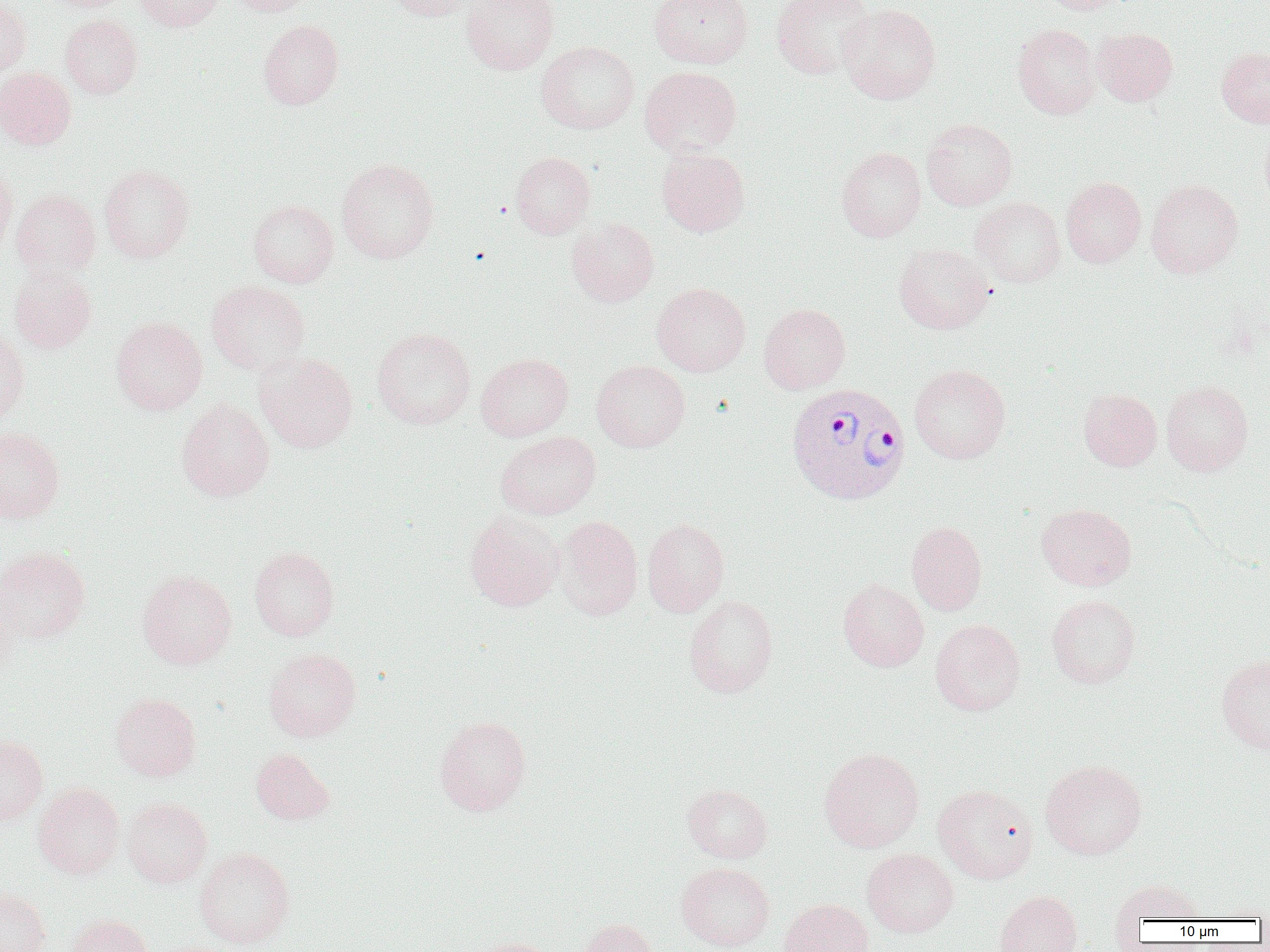

{
  "plasmodium_vivax_infected_red_blood_cell_locations": "approximate bounding boxes as (x1, y1, x2, y2) in pixels: (786, 382, 910, 505)",
  "slide_level_diagnosis": "Plasmodium vivax",
  "modality": "optical microscopy",
  "image_size": "1270×952 pixels",
  "preparation": "thin blood smear",
  "magnification": "1000x",
  "field_of_view": "single",
  "uninfected_red_blood_cell_locations": "approximate bounding boxes as (x1, y1, x2, y2) in pixels: (40, 0, 132, 12), (133, 0, 225, 31), (227, 0, 315, 16), (389, 0, 476, 21), (462, 0, 559, 75), (649, 0, 753, 69), (771, 0, 874, 79), (1039, 0, 1131, 15), (0, 1, 30, 80), (838, 3, 941, 104), (60, 14, 142, 99), (258, 19, 344, 109), (1013, 24, 1102, 118), (1092, 27, 1178, 106), (536, 41, 640, 134), (1216, 46, 1270, 127), (640, 66, 742, 157), (0, 67, 76, 150), (921, 118, 1017, 211), (1259, 119, 1270, 212), (837, 146, 926, 242), (656, 148, 750, 236), (510, 151, 595, 238), (337, 158, 439, 263), (99, 163, 195, 264), (0, 164, 17, 261), (1061, 177, 1146, 268), (1146, 179, 1243, 278), (11, 189, 101, 281), (970, 196, 1066, 288), (248, 199, 339, 287), (566, 218, 659, 307), (893, 243, 995, 334), (9, 267, 97, 354), (207, 280, 311, 375), (652, 282, 751, 376), (759, 303, 851, 393), (111, 317, 208, 414), (0, 325, 29, 423), (372, 328, 475, 429), (254, 352, 358, 453), (475, 353, 573, 441), (592, 360, 690, 452), (909, 363, 1011, 463), (1161, 381, 1253, 476), (1078, 388, 1162, 470), (176, 398, 274, 501), (0, 427, 65, 523), (495, 432, 601, 520), (1036, 503, 1136, 590), (464, 510, 564, 612), (554, 515, 643, 620), (642, 518, 730, 616), (906, 521, 987, 615), (0, 546, 90, 644), (249, 546, 339, 640), (137, 569, 237, 669), (837, 579, 928, 672), (0, 580, 19, 684), (684, 594, 778, 697), (1046, 594, 1140, 689), (930, 618, 1026, 716), (264, 647, 361, 742), (1216, 655, 1270, 753), (110, 692, 201, 781), (434, 715, 531, 816), (0, 733, 48, 827), (818, 747, 924, 852), (250, 748, 335, 825), (1040, 759, 1147, 860), (32, 783, 125, 880), (683, 783, 773, 863), (932, 784, 1039, 884), (122, 797, 212, 888), (195, 847, 295, 948), (862, 848, 959, 938), (676, 862, 775, 951), (1109, 879, 1207, 924), (0, 886, 51, 952), (994, 890, 1082, 952), (779, 898, 873, 952), (63, 913, 154, 952), (575, 918, 658, 952), (464, 937, 559, 952)"
}